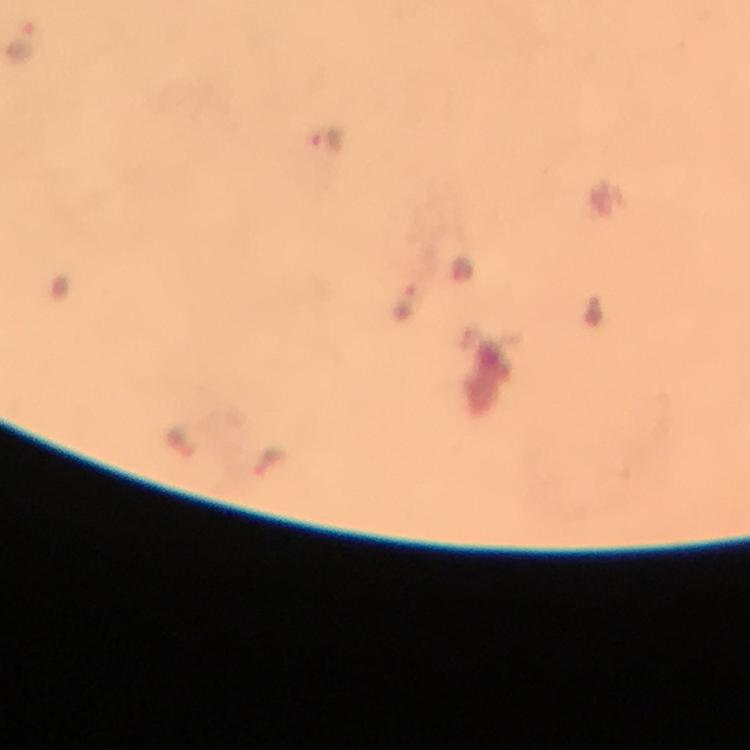
{
  "capture": "smartphone camera through the microscope",
  "cropped_from": "one field of view",
  "preparation": "thick blood smear",
  "magnification": "100x",
  "immersion_oil": "applied",
  "stain": "Giemsa",
  "context": "from a diagnostic examination for malaria",
  "image_size": "750×750 pixels",
  "plasmodium_parasite_locations": "approximate centers as (x, y) in pixels: (21, 44), (324, 140), (461, 270), (402, 301), (595, 311), (183, 445), (271, 458)"
}